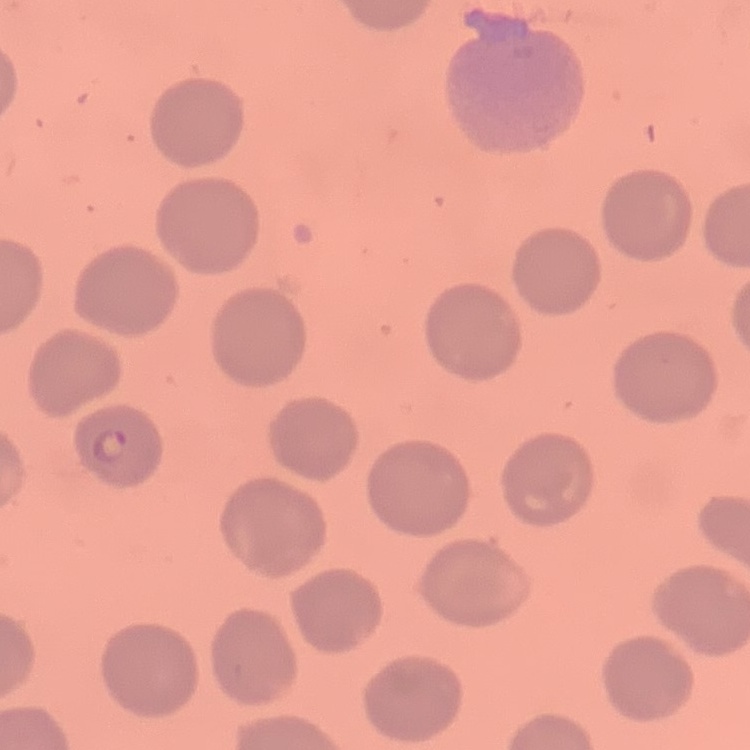

{
  "red_blood_cell_morphology": "no rouleaux formation",
  "preparation": "thin blood smear",
  "image_type": "square crop of a larger photomicrograph",
  "stain": "Field's or Giemsa"
}